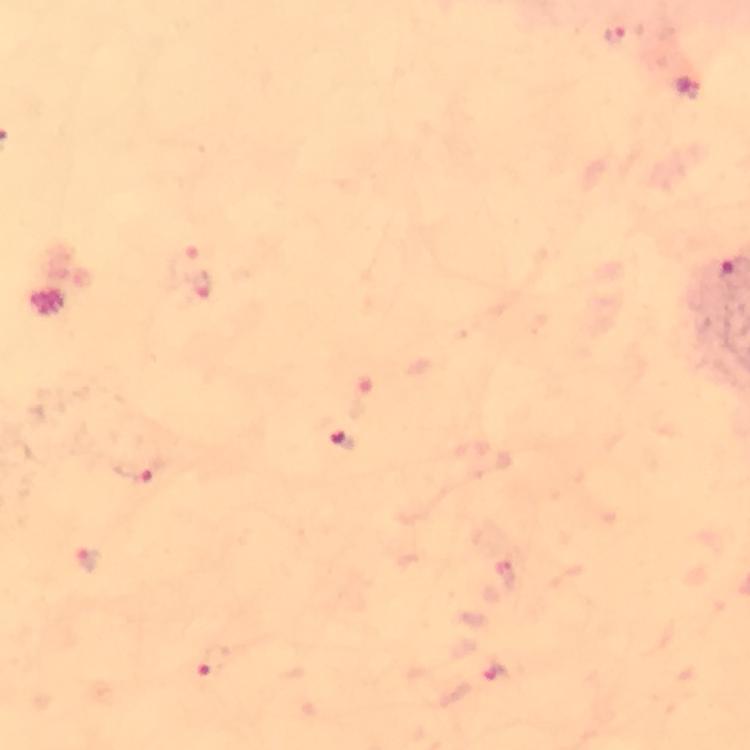

Approximate object centers, in pixels from the top-left corner. Malaria parasite locations: (x=623, y=36), (x=201, y=286), (x=341, y=438), (x=137, y=470), (x=88, y=558), (x=209, y=663), (x=495, y=671). From a diagnostic examination for malaria. Image is 750×750 pixels. At 100x magnification. Giemsa-stained preparation. Photographed through the microscope with a smartphone camera. Immersion oil was used. Cropped region of a single field of view. Thick blood smear.